Name the cell type shown.
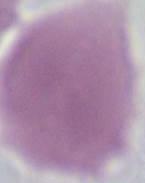

An erythrocyte.

Summary:
  - Modality: photomicrograph
  - Magnification: 1000x